Assess the morphology of the erythrocytes.
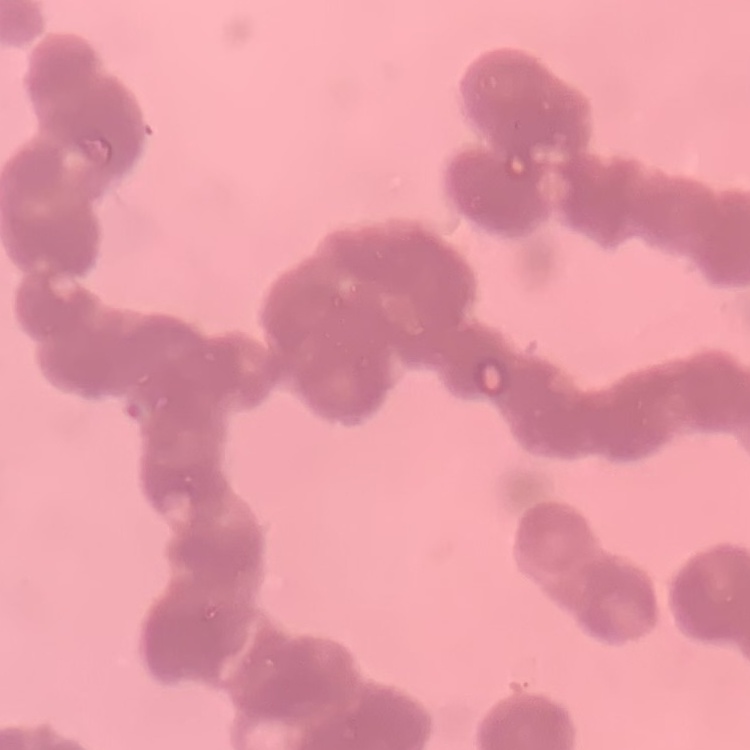
They show rouleaux formation.

Summary:
  - Image type: one tile cut from a larger photomicrograph
  - Stain: Field's or Giemsa
  - Preparation: thin blood film